Assess this cell for malaria.
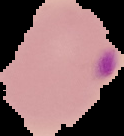

Parasitized.

Summary:
  - Preparation: thin blood smear
  - Image type: cell region segmented out of the field of view; surrounding area masked to black
  - Image size: 124×136 pixels